Report the malaria status of this cell.
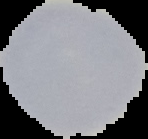
Uninfected.

Summary:
  - Image size: 148×139 pixels
  - Image type: cell region segmented out of the field of view; surrounding area masked to black
  - Preparation: thin blood film